Give the position of every Plasmodium parasite.
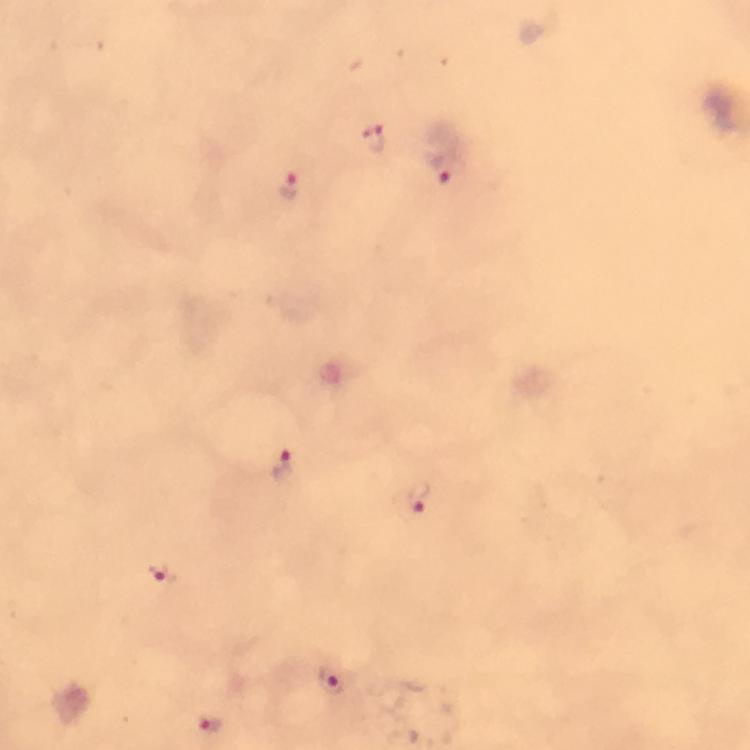

Approximate centers as {x, y} in pixels.
Plasmodium parasites: {374, 137}, {448, 169}, {288, 185}, {285, 465}, {419, 497}, {160, 573}, {334, 681}, {208, 725}.

preparation = thick blood smear
context = from a diagnostic examination for malaria
stain = Giemsa
immersion oil = used
magnification = 100x
image size = 750×750 pixels
cropped from = a single field of view
capture = smartphone mounted on the microscope